Assess this cell for malaria.
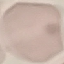
Uninfected.

Photographed with a smartphone camera at the microscope eyepiece. Thin blood smear. Giemsa stain. Cell patch, automatically extracted from a larger field of view and resized to 64 × 64 pixels.